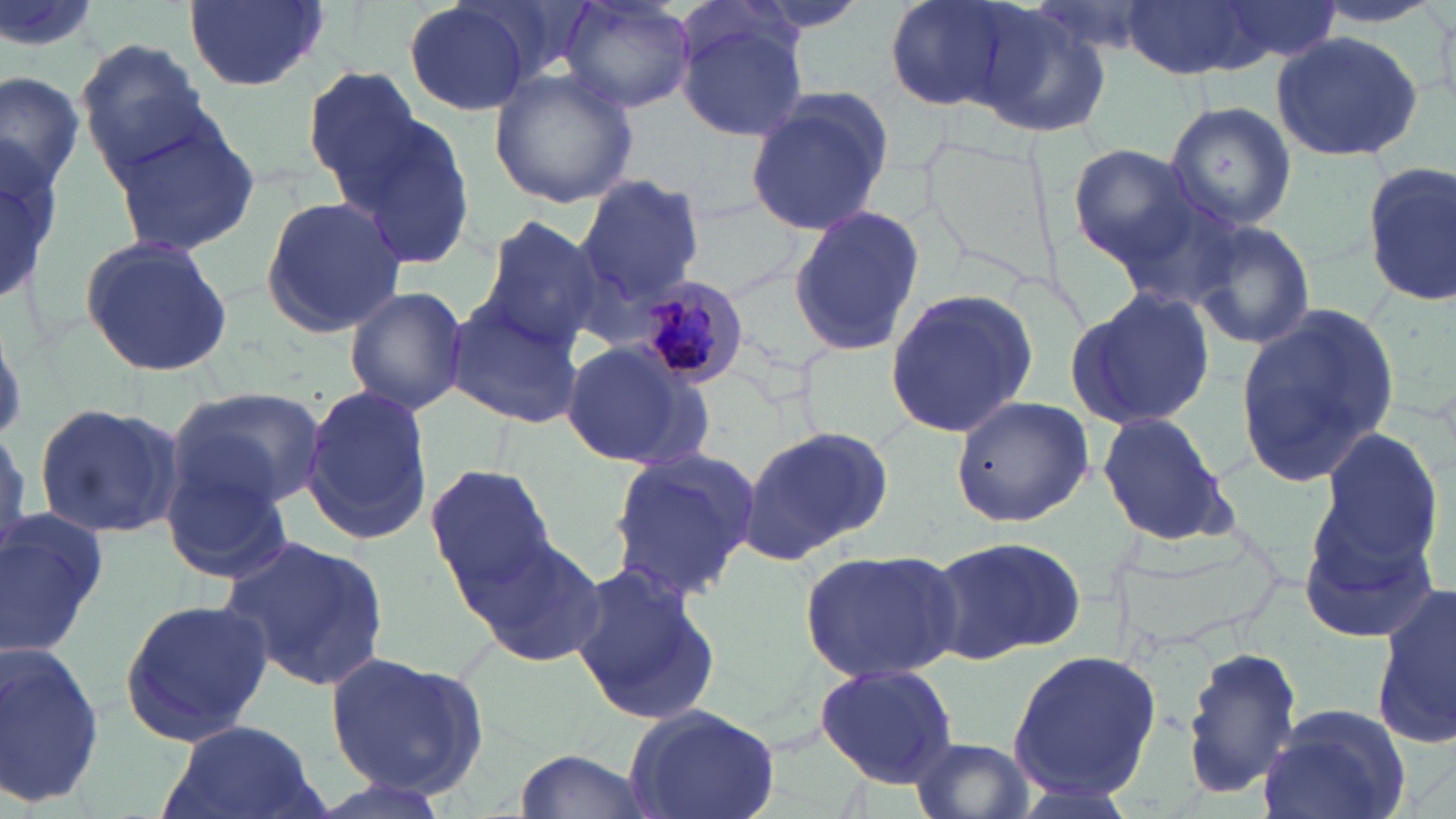
{
  "slide_level_diagnosis": "Plasmodium malariae",
  "stain": "May-Grünwald-Giemsa",
  "plasmodium_malariae_infected_red_blood_cell_locations": "approximate bounding boxes as (x1,y1)-(x2,y2) corner pairs in pixels: (638,276)-(751,387)",
  "magnification": "1000x",
  "image_size": "1456×819 pixels",
  "preparation": "thin blood smear",
  "uninfected_red_blood_cell_locations": "approximate bounding boxes as (x1,y1)-(x2,y2) corner pairs in pixels: (0,0)-(106,62), (184,0)-(328,92), (403,0)-(531,117), (557,0)-(698,114), (888,0)-(1035,112), (1118,0)-(1277,81), (1216,0)-(1339,66), (1302,2)-(1448,33), (1429,4)-(1456,115), (967,6)-(1116,139), (674,15)-(808,143), (1270,28)-(1423,163), (76,39)-(211,170), (304,66)-(427,188), (490,66)-(638,210), (0,70)-(84,199), (743,91)-(893,237), (1163,99)-(1296,231), (329,108)-(479,272), (103,111)-(261,257), (0,135)-(59,303), (1068,144)-(1202,265), (1361,158)-(1456,306), (574,175)-(704,309), (259,195)-(408,340), (1107,195)-(1251,312), (678,196)-(805,299), (790,207)-(928,357), (476,216)-(603,351), (1190,217)-(1318,352), (78,232)-(234,379), (344,285)-(468,416), (1067,287)-(1215,432), (883,289)-(1038,438), (443,299)-(586,427), (1234,305)-(1401,487), (561,339)-(708,468), (300,384)-(436,546), (166,387)-(326,510), (949,394)-(1094,527), (33,403)-(183,539), (1096,411)-(1237,548), (737,422)-(894,564), (1313,425)-(1449,575), (606,449)-(760,600), (159,459)-(295,585), (425,464)-(556,595), (1297,493)-(1439,642), (0,507)-(108,659), (462,529)-(607,670), (219,533)-(393,696), (924,533)-(1087,665), (797,545)-(967,685), (569,563)-(723,729), (1374,585)-(1456,749), (117,596)-(272,748), (0,644)-(105,807), (1181,645)-(1304,800), (1008,648)-(1162,800), (324,652)-(485,799), (815,662)-(958,789), (621,704)-(784,819), (1259,705)-(1415,819), (164,719)-(322,819), (909,735)-(1037,819), (510,747)-(656,819), (995,777)-(1147,819)",
  "modality": "light microscopy",
  "field_of_view": "one of a larger specimen"
}